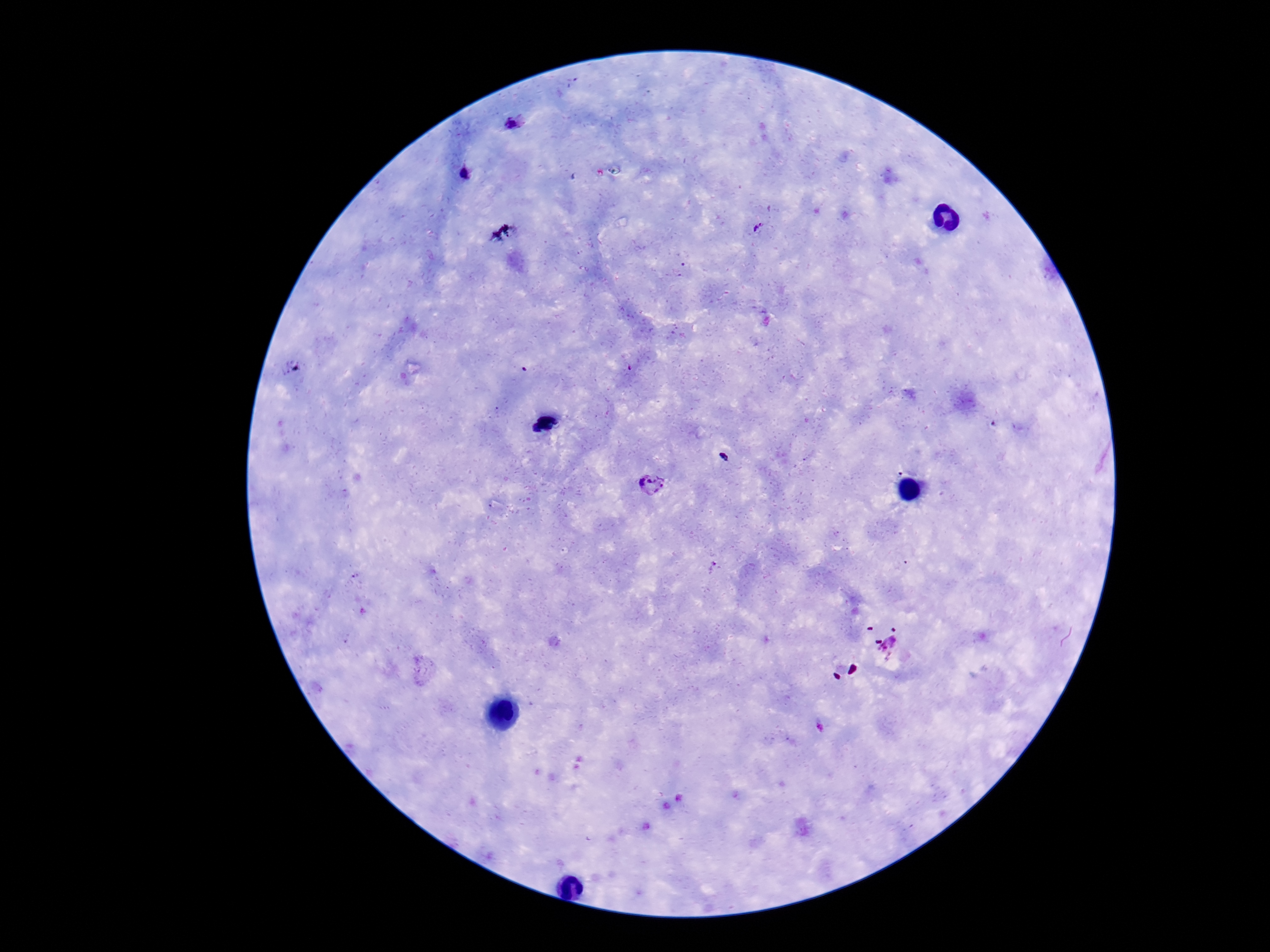

Approximate object centers, in pixels from the top-left corner.
Summary:
  - Plasmodium parasite locations: (x=513, y=124), (x=466, y=173), (x=760, y=230), (x=652, y=486), (x=895, y=648)
  - Capture: smartphone camera through the microscope eyepiece
  - Preparation: thick blood film
  - Magnification: 100x
  - Stain: Giemsa
  - Patient malaria status: positive
  - Field of view: single
  - Image size: 1270×952 pixels